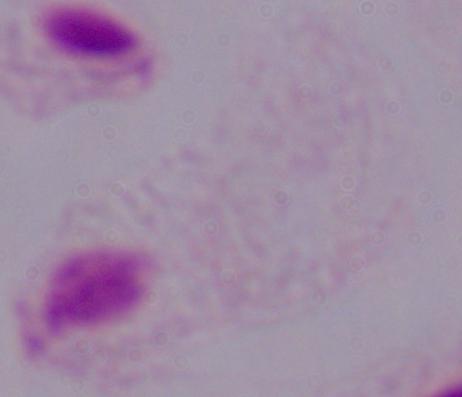

magnification: 1000x
identification: trichomonad
modality: micrograph